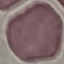
{
  "malaria_status": "uninfected",
  "preparation": "thin blood film",
  "stain": "Giemsa",
  "image_type": "cell patch, automatically extracted from a larger field of view and resized to 64 × 64 pixels",
  "capture": "smartphone camera at the microscope eyepiece"
}